Locate every blood parasite and identify its species.
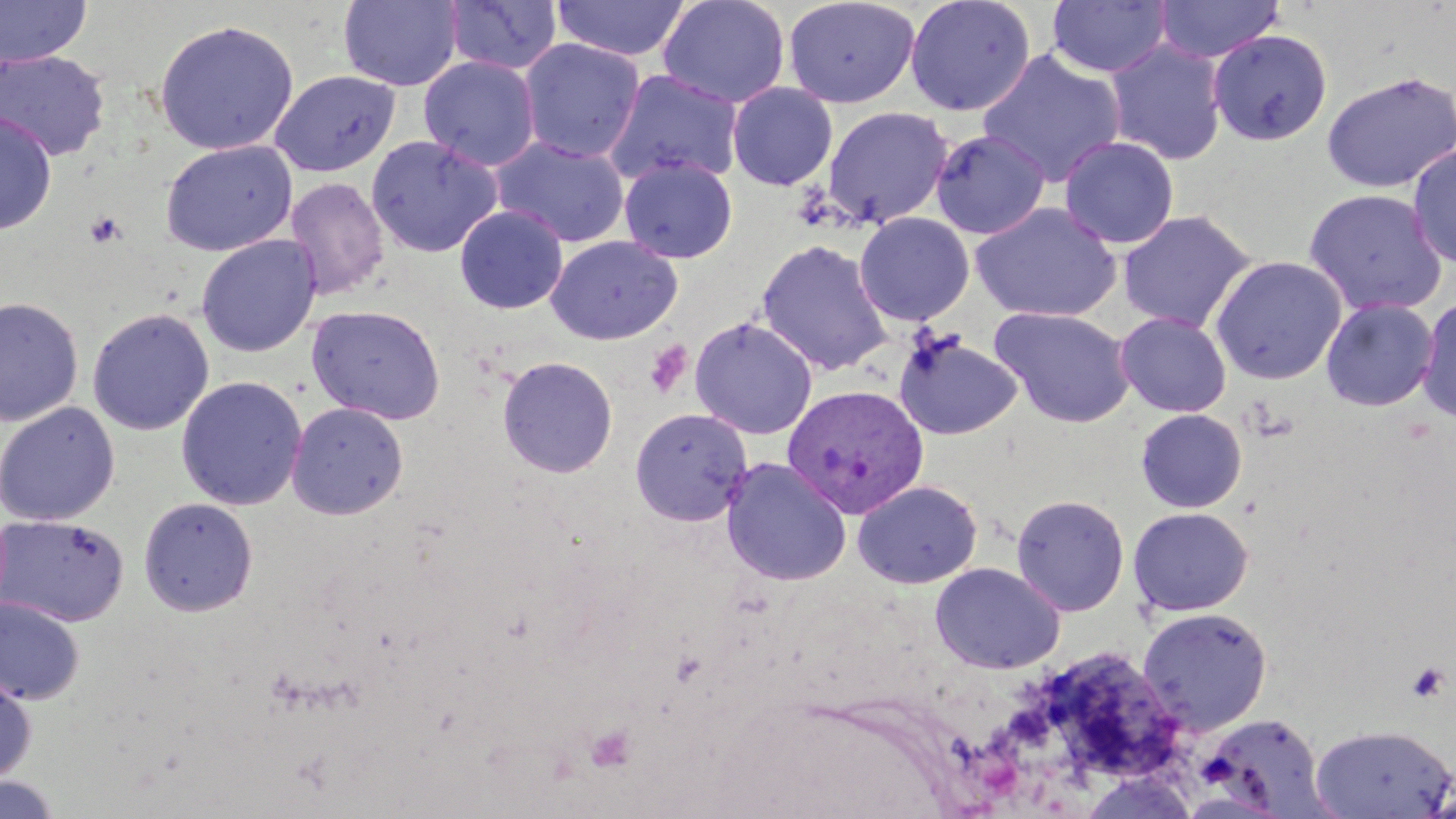

Approximate bounding boxes as named x1/y1/x2/y2 corners in pixels.
Plasmodium vivax-infected red blood cells: (x1=779, y1=384, x2=927, y2=519).
No Plasmodium falciparum, Plasmodium ovale, Plasmodium malariae, Babesia divergens, or Trypanosoma brucei observed.

slide-level diagnosis = Plasmodium vivax
modality = light microscopy
image size = 1456×819 pixels
preparation = thin blood smear
field of view = single
platelet locations = approximate bounding boxes as named x1/y1/x2/y2 corners in pixels: (x1=84, y1=210, x2=128, y2=248), (x1=644, y1=341, x2=692, y2=398), (x1=1406, y1=662, x2=1450, y2=703), (x1=585, y1=724, x2=637, y2=771)
stain = May-Grünwald-Giemsa
uninfected red blood cell locations = approximate bounding boxes as named x1/y1/x2/y2 corners in pixels: (x1=0, y1=0, x2=93, y2=67), (x1=443, y1=0, x2=562, y2=75), (x1=551, y1=0, x2=691, y2=61), (x1=658, y1=0, x2=791, y2=109), (x1=783, y1=0, x2=919, y2=108), (x1=904, y1=0, x2=1036, y2=117), (x1=1153, y1=0, x2=1284, y2=64), (x1=337, y1=1, x2=463, y2=91), (x1=1047, y1=1, x2=1172, y2=79), (x1=153, y1=19, x2=299, y2=155), (x1=1208, y1=29, x2=1332, y2=146), (x1=519, y1=39, x2=645, y2=162), (x1=1105, y1=39, x2=1227, y2=166), (x1=0, y1=49, x2=111, y2=162), (x1=976, y1=49, x2=1127, y2=188), (x1=418, y1=56, x2=540, y2=171), (x1=604, y1=69, x2=744, y2=188), (x1=269, y1=70, x2=401, y2=177), (x1=1320, y1=70, x2=1456, y2=193), (x1=727, y1=82, x2=838, y2=190), (x1=822, y1=105, x2=953, y2=228), (x1=0, y1=112, x2=57, y2=236), (x1=930, y1=129, x2=1050, y2=239), (x1=366, y1=135, x2=502, y2=257), (x1=1059, y1=135, x2=1180, y2=249), (x1=491, y1=137, x2=630, y2=248), (x1=160, y1=139, x2=297, y2=257), (x1=1407, y1=144, x2=1456, y2=269), (x1=620, y1=157, x2=737, y2=263), (x1=285, y1=177, x2=389, y2=301), (x1=1303, y1=188, x2=1449, y2=316), (x1=970, y1=202, x2=1122, y2=322), (x1=454, y1=205, x2=568, y2=314), (x1=1117, y1=208, x2=1258, y2=333), (x1=854, y1=212, x2=975, y2=326), (x1=196, y1=235, x2=321, y2=357), (x1=546, y1=235, x2=682, y2=345), (x1=756, y1=239, x2=893, y2=375), (x1=1209, y1=255, x2=1348, y2=385), (x1=0, y1=296, x2=84, y2=427), (x1=1320, y1=296, x2=1439, y2=412), (x1=1417, y1=296, x2=1456, y2=425), (x1=306, y1=304, x2=446, y2=424), (x1=989, y1=306, x2=1135, y2=427), (x1=87, y1=307, x2=214, y2=436), (x1=1115, y1=311, x2=1232, y2=417), (x1=689, y1=316, x2=818, y2=439), (x1=894, y1=331, x2=1022, y2=441), (x1=497, y1=356, x2=618, y2=478), (x1=175, y1=376, x2=307, y2=510), (x1=0, y1=402, x2=120, y2=526), (x1=287, y1=402, x2=408, y2=520), (x1=629, y1=407, x2=753, y2=526), (x1=1135, y1=408, x2=1247, y2=513), (x1=720, y1=458, x2=852, y2=586), (x1=852, y1=479, x2=983, y2=588), (x1=1010, y1=494, x2=1130, y2=616), (x1=138, y1=497, x2=257, y2=615), (x1=1127, y1=506, x2=1254, y2=616), (x1=0, y1=514, x2=129, y2=628), (x1=930, y1=561, x2=1066, y2=674), (x1=0, y1=597, x2=85, y2=705), (x1=1137, y1=606, x2=1274, y2=735), (x1=1044, y1=653, x2=1185, y2=781), (x1=0, y1=670, x2=36, y2=786), (x1=1199, y1=712, x2=1332, y2=817), (x1=1310, y1=724, x2=1455, y2=817), (x1=1078, y1=770, x2=1201, y2=818), (x1=0, y1=774, x2=63, y2=819)
magnification = 1000x